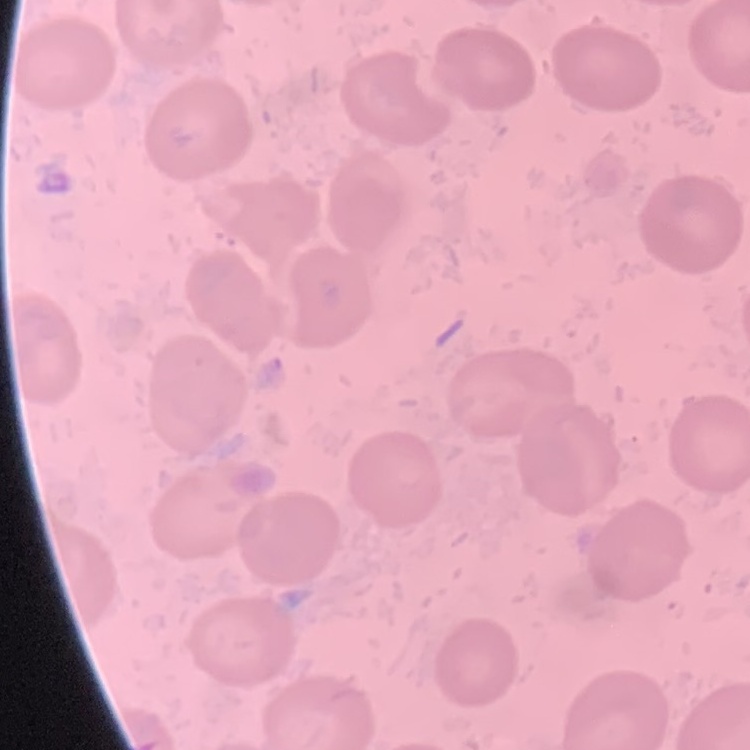

The red blood cells exhibit no rouleaux formation. Thin blood smear. Square crop of a larger photomicrograph. Stained with either Field's or Giemsa.